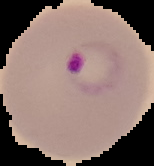
image_type: cell region segmented out of the field of view; surrounding area masked to black
malaria_status: parasitized
preparation: thin blood smear
image_size: 154×166 pixels